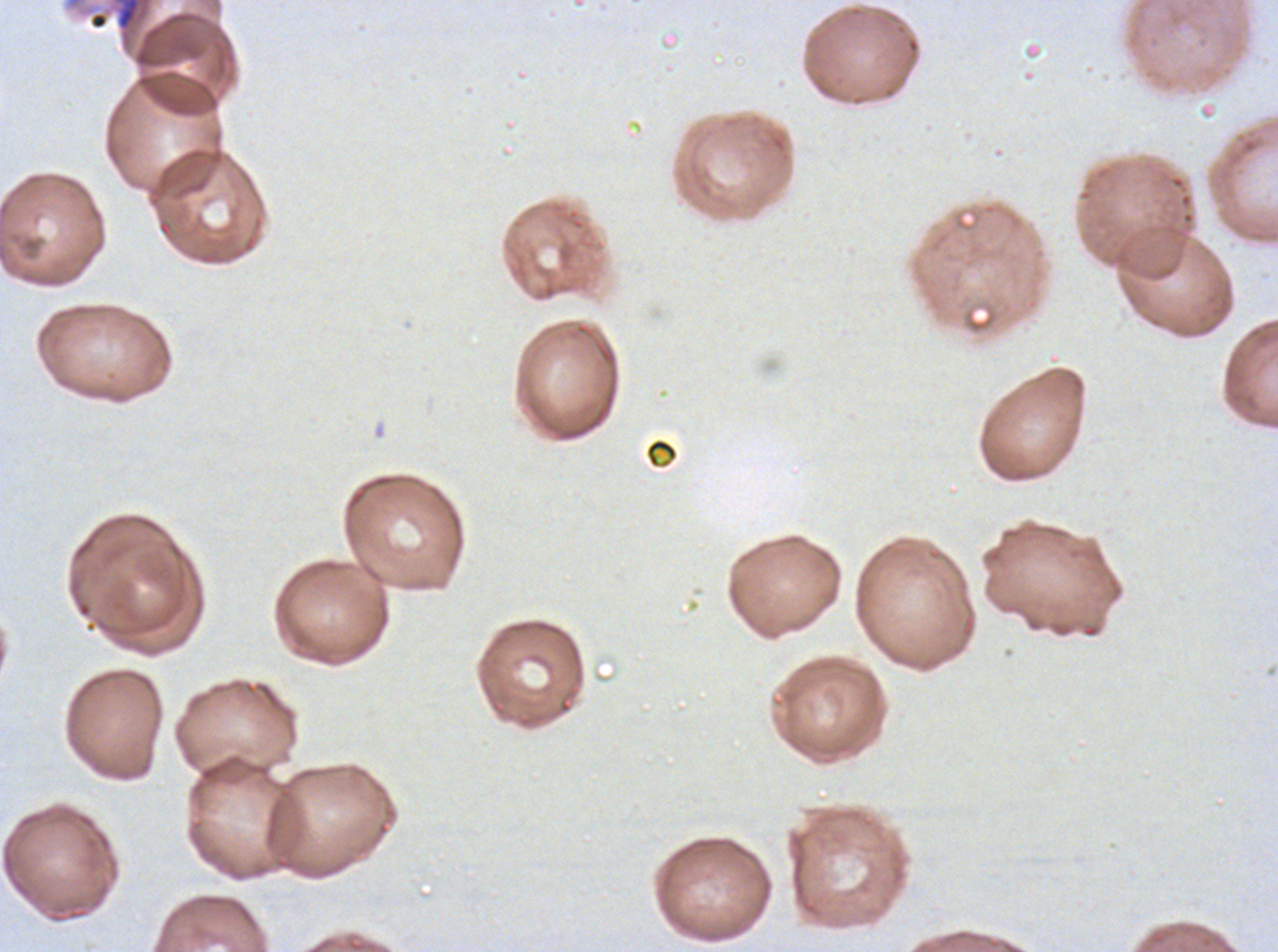
notation = approximate bounding rectangles given as corner coordinates in pixels from the top-left
debris locations = (x1=90, y1=12, x2=108, y2=30), (x1=644, y1=437, x2=679, y2=470)
stain = Giemsa
specimen = P. falciparum from a patient in The Gambia, cultured ex vivo for 24 to 48 hours
preparation = thin blood film
image size = 1278×952 pixels
field of view = one sub-image of a larger composite